Name the parasite shown.
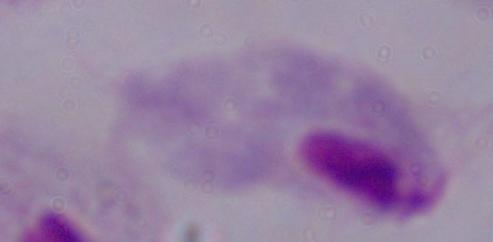
A trichomonad.

modality = micrograph
magnification = 1000x